Report the malaria status of this cell.
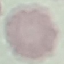
It is uninfected.

Summary:
  - Capture: smartphone camera at the microscope eyepiece
  - Image type: automatically extracted cell patch, resized to 64 × 64 pixels
  - Preparation: thin smear
  - Stain: Giemsa